Identify the blood parasite species.
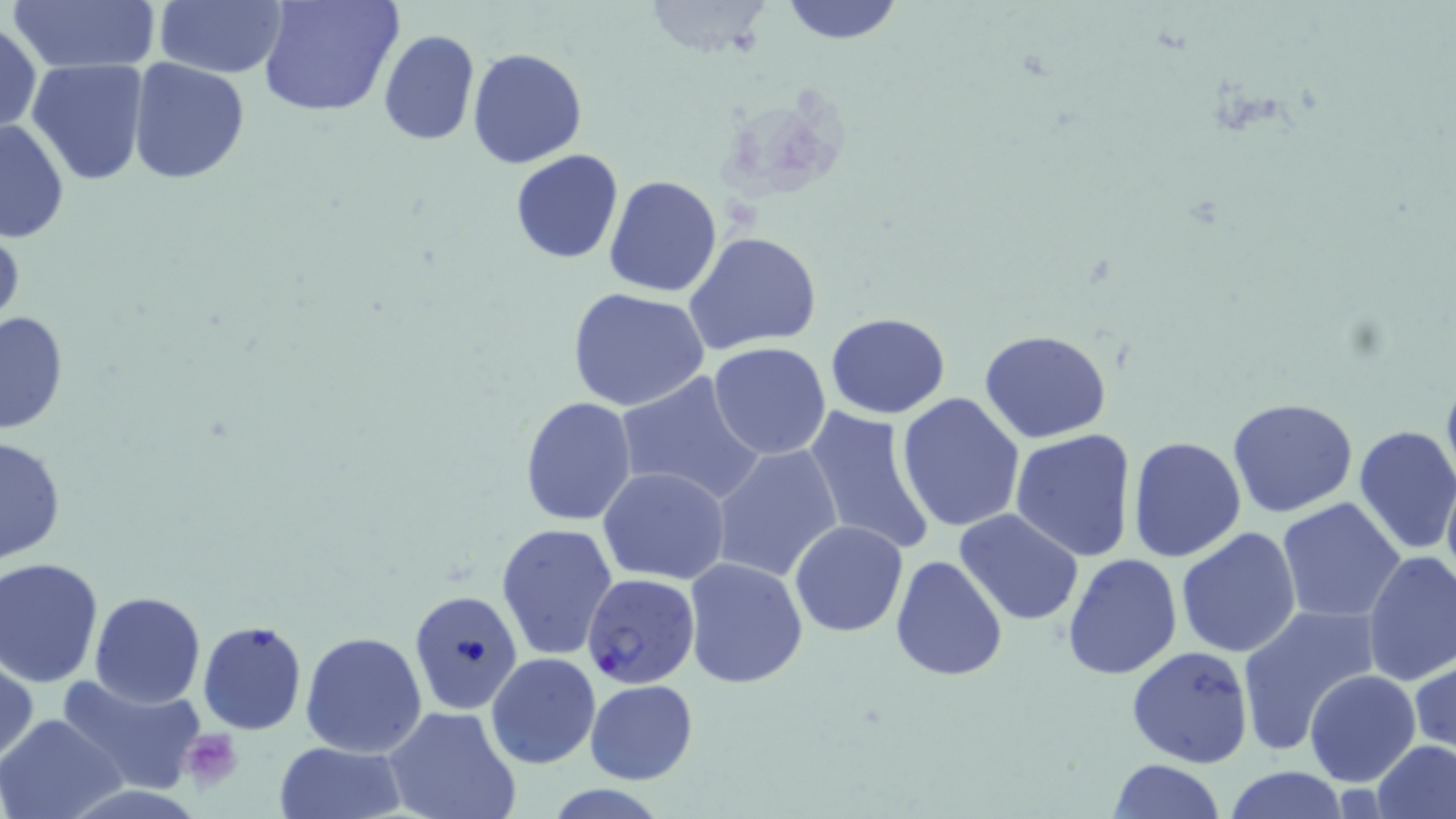

Plasmodium falciparum.

{
  "magnification": "1000x",
  "stain": "May-Grünwald-Giemsa",
  "image_size": "1456×819 pixels",
  "platelet_locations": "approximate bounding boxes as named x1/y1/x2/y2 corners in pixels: (x1=176, y1=730, x2=244, y2=791)",
  "preparation": "thin blood smear",
  "uninfected_red_blood_cell_locations": "approximate bounding boxes as named x1/y1/x2/y2 corners in pixels: (x1=153, y1=0, x2=289, y2=78), (x1=257, y1=0, x2=405, y2=119), (x1=639, y1=0, x2=771, y2=59), (x1=777, y1=0, x2=906, y2=46), (x1=13, y1=1, x2=158, y2=74), (x1=0, y1=18, x2=43, y2=136), (x1=377, y1=30, x2=480, y2=146), (x1=467, y1=48, x2=589, y2=169), (x1=27, y1=58, x2=149, y2=185), (x1=129, y1=58, x2=251, y2=186), (x1=0, y1=119, x2=70, y2=243), (x1=510, y1=149, x2=624, y2=265), (x1=603, y1=174, x2=723, y2=297), (x1=0, y1=225, x2=24, y2=337), (x1=684, y1=232, x2=822, y2=353), (x1=567, y1=287, x2=710, y2=412), (x1=0, y1=309, x2=70, y2=435), (x1=826, y1=312, x2=949, y2=419), (x1=979, y1=329, x2=1112, y2=443), (x1=708, y1=341, x2=832, y2=459), (x1=614, y1=371, x2=765, y2=505), (x1=897, y1=393, x2=1026, y2=533), (x1=1228, y1=396, x2=1359, y2=518), (x1=520, y1=397, x2=637, y2=523), (x1=804, y1=406, x2=939, y2=559), (x1=1353, y1=424, x2=1456, y2=558), (x1=1010, y1=429, x2=1137, y2=562), (x1=0, y1=434, x2=67, y2=565), (x1=1127, y1=437, x2=1246, y2=562), (x1=711, y1=444, x2=843, y2=583), (x1=598, y1=466, x2=731, y2=584), (x1=1441, y1=472, x2=1456, y2=595), (x1=1276, y1=497, x2=1407, y2=624), (x1=954, y1=510, x2=1084, y2=626), (x1=789, y1=520, x2=908, y2=637), (x1=495, y1=522, x2=619, y2=664), (x1=1174, y1=528, x2=1301, y2=657), (x1=1363, y1=550, x2=1456, y2=685), (x1=1063, y1=553, x2=1183, y2=680), (x1=892, y1=555, x2=1008, y2=682), (x1=682, y1=556, x2=810, y2=690), (x1=0, y1=559, x2=104, y2=688), (x1=89, y1=591, x2=206, y2=708), (x1=1236, y1=601, x2=1382, y2=753), (x1=197, y1=619, x2=307, y2=736), (x1=300, y1=630, x2=427, y2=759), (x1=1127, y1=645, x2=1253, y2=767), (x1=485, y1=652, x2=601, y2=769), (x1=1, y1=656, x2=38, y2=769), (x1=1411, y1=657, x2=1455, y2=754), (x1=1304, y1=669, x2=1421, y2=786), (x1=55, y1=672, x2=207, y2=797), (x1=585, y1=680, x2=698, y2=785), (x1=382, y1=707, x2=522, y2=819), (x1=0, y1=713, x2=124, y2=819), (x1=1373, y1=739, x2=1456, y2=819), (x1=274, y1=741, x2=407, y2=819), (x1=1108, y1=759, x2=1225, y2=818), (x1=1221, y1=765, x2=1348, y2=819)",
  "field_of_view": "one of a larger specimen",
  "plasmodium_falciparum_infected_red_blood_cell_locations": "approximate bounding boxes as named x1/y1/x2/y2 corners in pixels: (x1=582, y1=573, x2=702, y2=690), (x1=409, y1=590, x2=527, y2=713)",
  "modality": "optical microscopy"
}